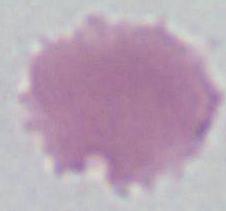

identification = erythrocyte
magnification = 1000x
modality = micrograph